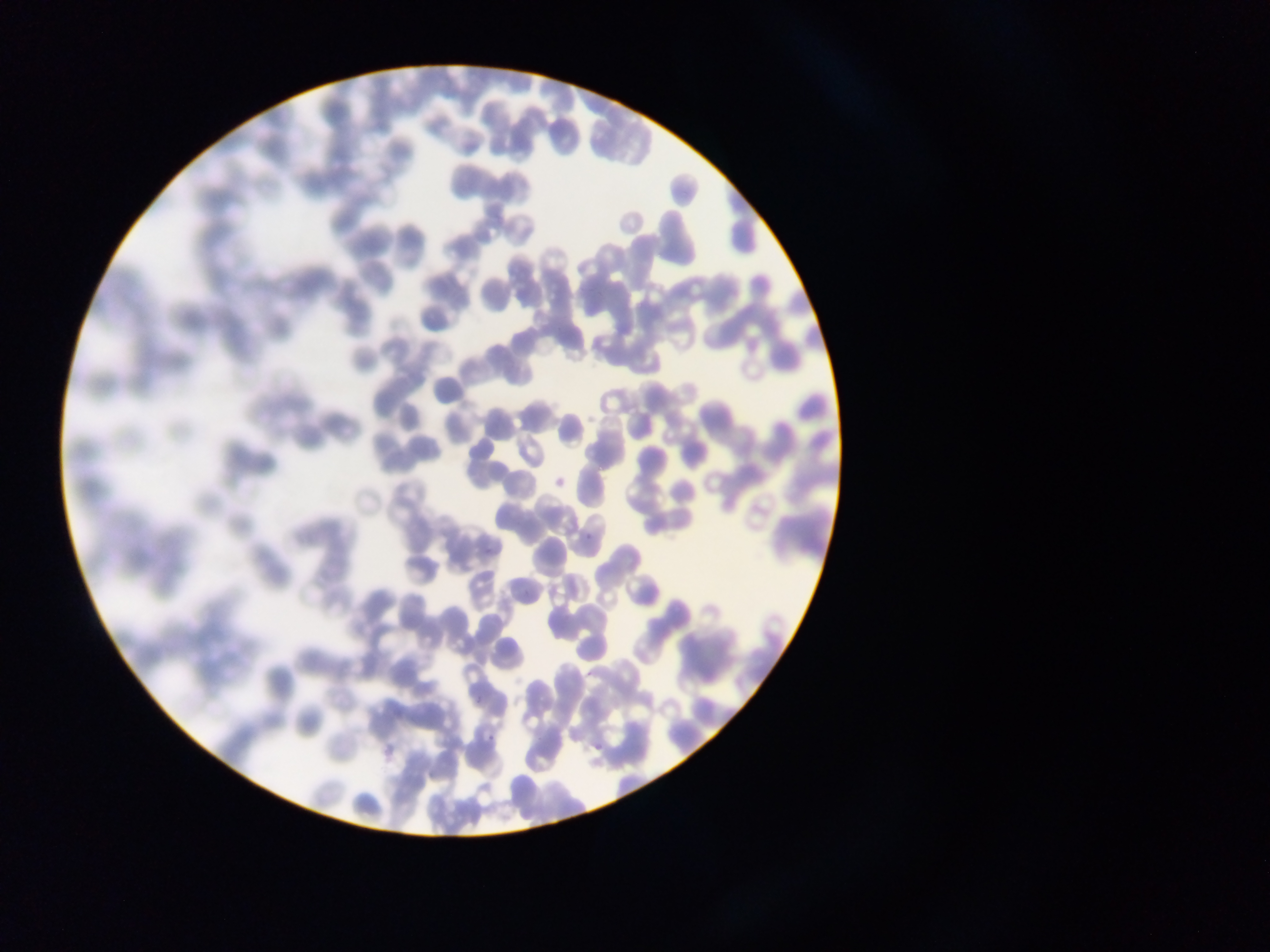
Approximate bounding boxes as left top right bottom in pixels.
Summary:
  - Malaria parasite locations: 583 528 596 543; 475 684 485 710; 487 736 496 745; 596 741 602 754
  - Image size: 1270×952 pixels
  - Preparation: thin blood film
  - Field of view: single
  - Capture: mobile-phone photograph through a microscope
  - Country: Ghana